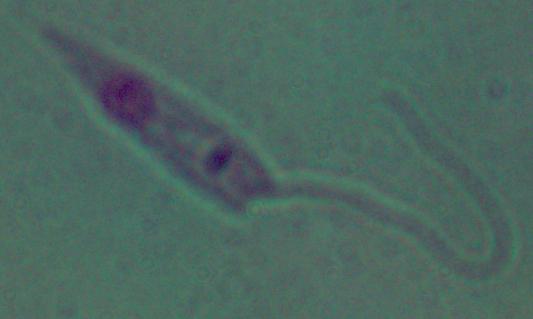 Micrograph. A Leishmania parasite is shown. Captured at 1000x magnification.